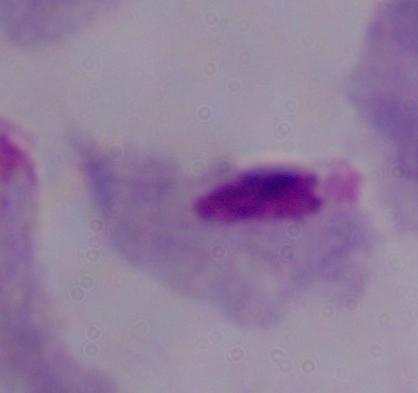
A trichomonad is shown. Photomicrograph. 1000x magnification.